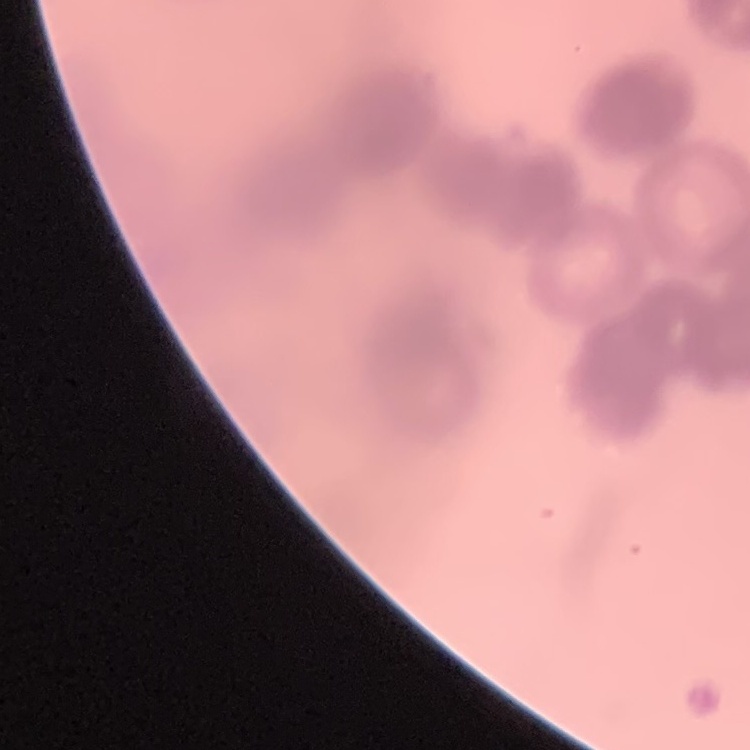

Summary:
  - Erythrocyte morphology: rouleaux formation
  - Image type: square crop of a larger photomicrograph
  - Preparation: thin blood film
  - Stain: Field's or Giemsa